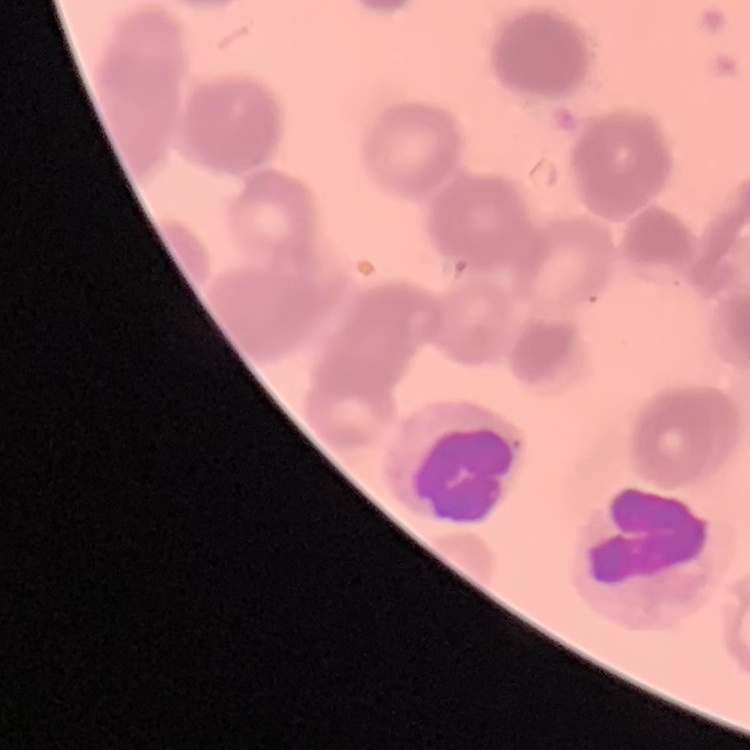
erythrocyte morphology = rouleaux formation
image type = one tile cut from a larger photomicrograph
preparation = thin blood film
stain = Field's or Giemsa